State which parasite is depicted.
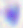
Toxoplasma gondii.

Summary:
  - Magnification: 400x
  - Modality: micrograph